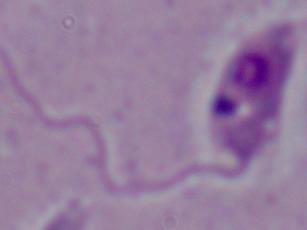

Summary:
  - Magnification: 1000x
  - Identification: Leishmania
  - Modality: micrograph